Assess the morphology of the red blood cells.
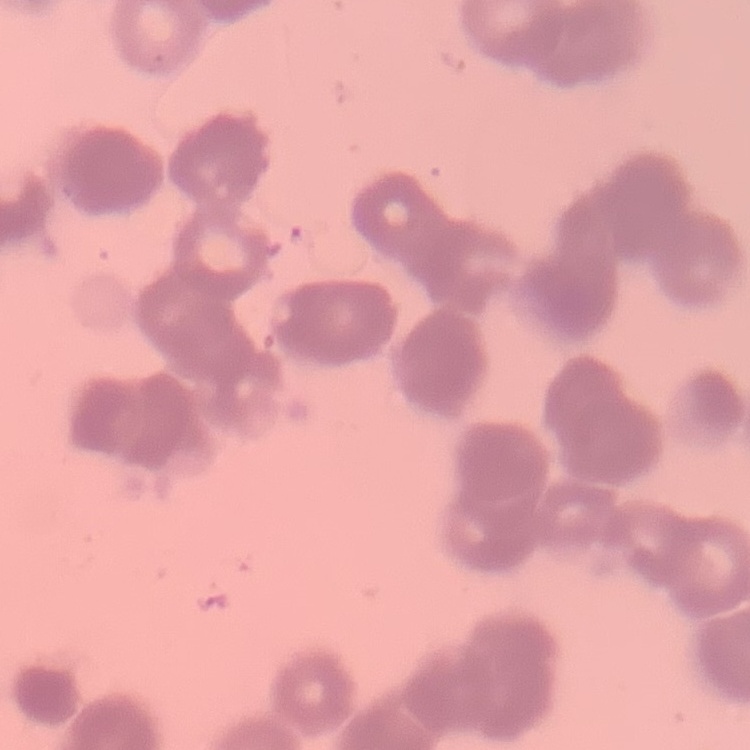

Rouleaux formation.

Stained with either Field's or Giemsa. Square crop of a larger photomicrograph. Thin blood smear.